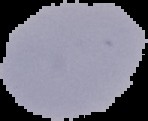

preparation = thin blood film
image size = 148×121 pixels
image type = segmented cell region with the area outside set to black
malaria status = uninfected